Assess the morphology of the erythrocytes.
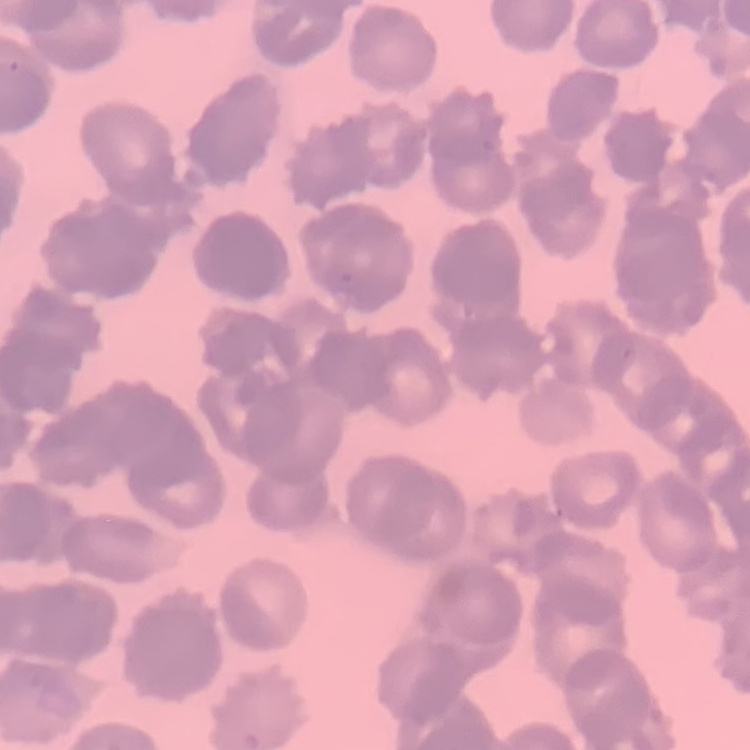

They show rouleaux formation.

Stained with either Field's or Giemsa. Thin blood film. Square crop of a larger photomicrograph.